Identify the blood parasite species.
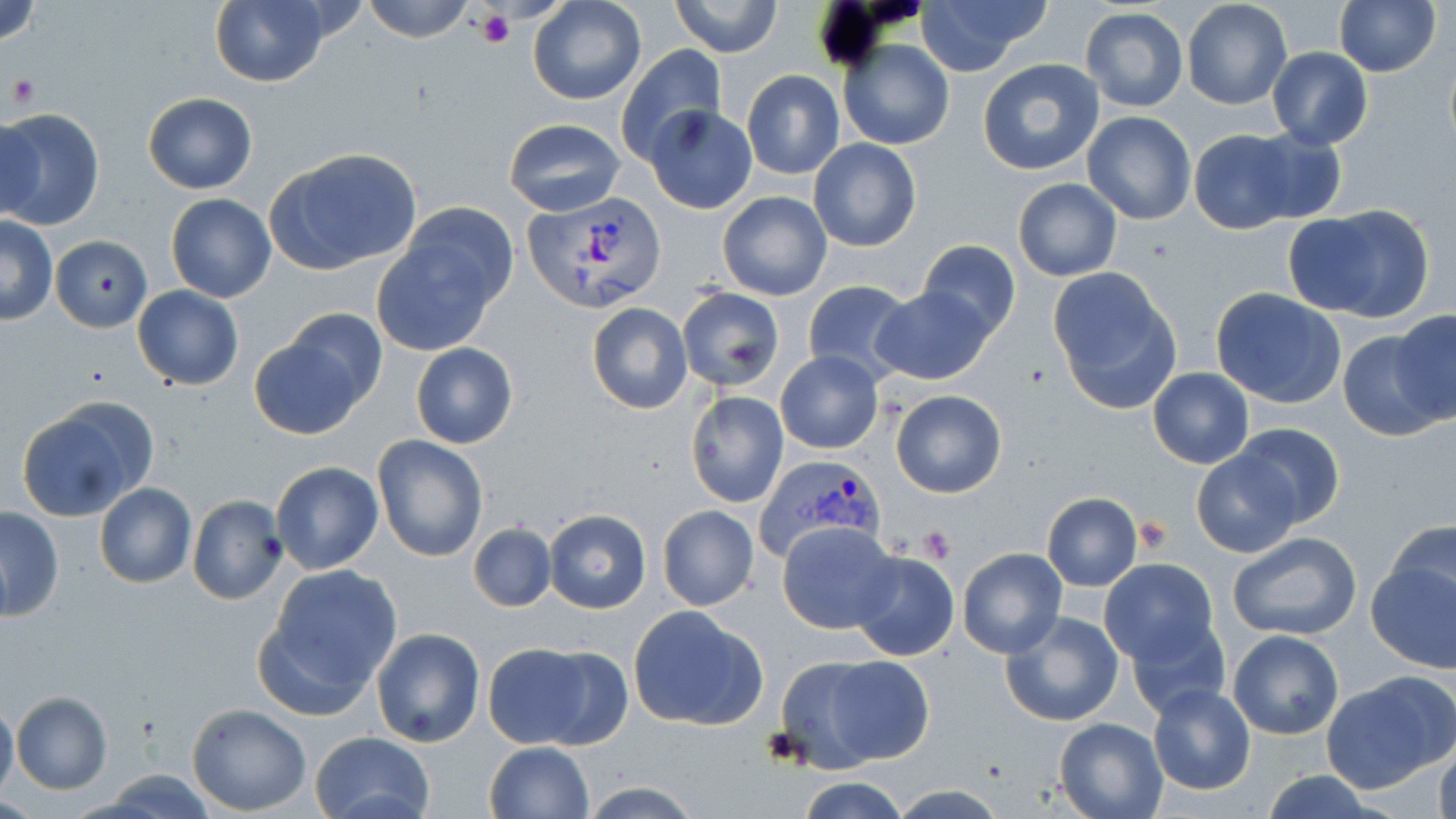

Plasmodium vivax.

Approximate bounding boxes as named x1/y1/x2/y2 corners in pixels. Uninfected red blood cell locations: (x1=0, y1=0, x2=44, y2=46), (x1=362, y1=0, x2=475, y2=43), (x1=527, y1=0, x2=647, y2=107), (x1=915, y1=0, x2=1049, y2=77), (x1=1335, y1=0, x2=1441, y2=76), (x1=209, y1=1, x2=331, y2=87), (x1=672, y1=1, x2=782, y2=57), (x1=1182, y1=1, x2=1291, y2=111), (x1=1080, y1=7, x2=1189, y2=112), (x1=839, y1=39, x2=955, y2=150), (x1=616, y1=45, x2=726, y2=163), (x1=1267, y1=47, x2=1372, y2=149), (x1=976, y1=58, x2=1105, y2=176), (x1=741, y1=71, x2=845, y2=180), (x1=142, y1=93, x2=258, y2=194), (x1=646, y1=105, x2=757, y2=214), (x1=0, y1=108, x2=103, y2=229), (x1=1082, y1=112, x2=1196, y2=224), (x1=0, y1=117, x2=45, y2=220), (x1=504, y1=118, x2=628, y2=217), (x1=1242, y1=128, x2=1348, y2=224), (x1=1186, y1=129, x2=1305, y2=234), (x1=808, y1=138, x2=921, y2=251), (x1=266, y1=148, x2=423, y2=274), (x1=1013, y1=177, x2=1122, y2=281), (x1=717, y1=191, x2=832, y2=302), (x1=166, y1=194, x2=276, y2=303), (x1=402, y1=203, x2=517, y2=308), (x1=1283, y1=203, x2=1437, y2=325), (x1=1, y1=218, x2=57, y2=324), (x1=372, y1=223, x2=506, y2=355), (x1=51, y1=236, x2=152, y2=332), (x1=917, y1=239, x2=1020, y2=341), (x1=1047, y1=268, x2=1181, y2=415), (x1=801, y1=279, x2=914, y2=384), (x1=871, y1=285, x2=997, y2=385), (x1=132, y1=287, x2=243, y2=391), (x1=676, y1=287, x2=784, y2=393), (x1=1210, y1=287, x2=1347, y2=409), (x1=586, y1=302, x2=692, y2=414), (x1=284, y1=309, x2=387, y2=409), (x1=1392, y1=309, x2=1456, y2=425), (x1=249, y1=327, x2=375, y2=439), (x1=1337, y1=328, x2=1450, y2=441), (x1=410, y1=343, x2=519, y2=449), (x1=777, y1=350, x2=884, y2=454), (x1=1148, y1=367, x2=1254, y2=468), (x1=891, y1=390, x2=1007, y2=498), (x1=685, y1=391, x2=789, y2=508), (x1=15, y1=399, x2=155, y2=522), (x1=1232, y1=423, x2=1345, y2=528), (x1=373, y1=436, x2=488, y2=560), (x1=1190, y1=451, x2=1299, y2=557), (x1=269, y1=461, x2=384, y2=574), (x1=95, y1=484, x2=196, y2=588), (x1=1041, y1=492, x2=1143, y2=592), (x1=187, y1=494, x2=288, y2=605), (x1=657, y1=504, x2=760, y2=611), (x1=0, y1=506, x2=63, y2=622), (x1=544, y1=508, x2=651, y2=612), (x1=1384, y1=519, x2=1456, y2=625), (x1=778, y1=521, x2=899, y2=633), (x1=468, y1=523, x2=556, y2=612), (x1=1226, y1=531, x2=1364, y2=641), (x1=957, y1=547, x2=1068, y2=659), (x1=1364, y1=548, x2=1456, y2=675), (x1=848, y1=551, x2=959, y2=661), (x1=1098, y1=558, x2=1220, y2=666), (x1=263, y1=564, x2=402, y2=701), (x1=628, y1=604, x2=768, y2=731), (x1=1000, y1=611, x2=1126, y2=728), (x1=1125, y1=616, x2=1231, y2=721), (x1=371, y1=627, x2=484, y2=748), (x1=1228, y1=630, x2=1344, y2=739), (x1=482, y1=643, x2=600, y2=749), (x1=532, y1=647, x2=634, y2=749), (x1=791, y1=650, x2=936, y2=766), (x1=1324, y1=671, x2=1455, y2=793), (x1=1147, y1=685, x2=1256, y2=796), (x1=10, y1=692, x2=112, y2=794), (x1=0, y1=698, x2=18, y2=804), (x1=186, y1=704, x2=310, y2=816), (x1=1055, y1=717, x2=1169, y2=819), (x1=309, y1=730, x2=435, y2=819), (x1=1431, y1=736, x2=1456, y2=819), (x1=486, y1=742, x2=593, y2=818), (x1=1255, y1=771, x2=1379, y2=819), (x1=795, y1=777, x2=912, y2=819), (x1=575, y1=780, x2=706, y2=819), (x1=884, y1=784, x2=1010, y2=819). Plasmodium vivax-infected red blood cell locations: (x1=526, y1=191, x2=669, y2=316), (x1=758, y1=455, x2=884, y2=561). Platelet locations: (x1=476, y1=10, x2=513, y2=49), (x1=5, y1=74, x2=40, y2=110), (x1=1131, y1=515, x2=1172, y2=555), (x1=917, y1=525, x2=956, y2=564). One field of a larger specimen. May-Grünwald-Giemsa stain. Thin blood smear. 1000x magnification. Image is 1456×819 pixels. Optical microscopy.